Report the malaria status of this cell.
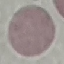
Uninfected.

Giemsa stain. Photographed with a smartphone camera at the microscope eyepiece. Thin blood film. Automatically extracted cell patch, resized to 64 × 64 pixels.